Assess this cell for malaria.
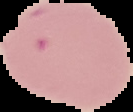
It is parasitized.

{
  "preparation": "thin blood smear",
  "image_type": "segmented cell region on a black background",
  "image_size": "133×112 pixels"
}